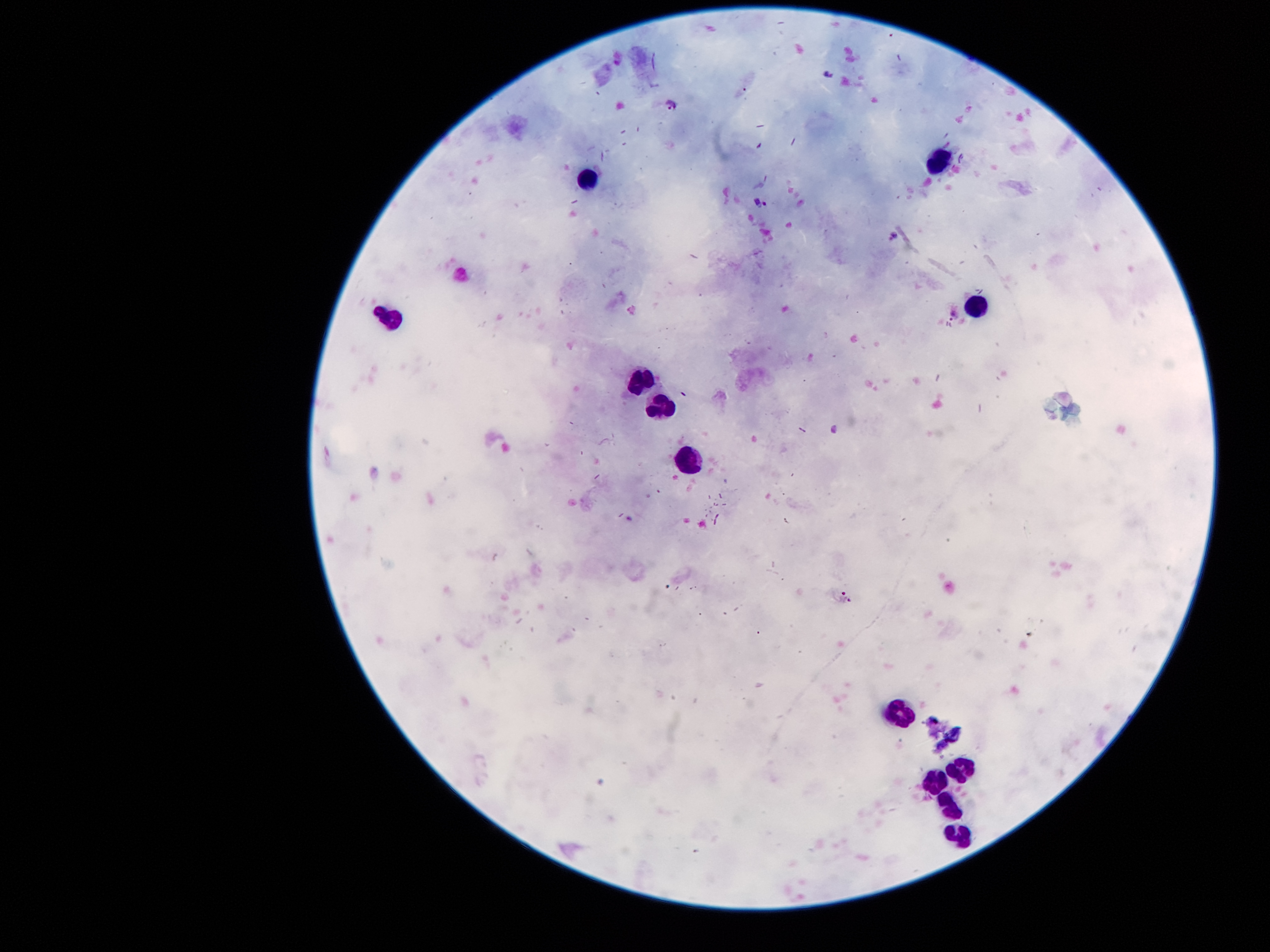

{
  "capture": "smartphone through the microscope eyepiece",
  "stain": "Giemsa",
  "preparation": "thick peripheral-blood smear",
  "patient_malaria_status": "infected with Plasmodium falciparum",
  "leukocyte_locations": "approximate centers as {x, y} in pixels: {937, 161}, {586, 176}, {978, 304}, {390, 316}, {639, 377}, {662, 405}, {695, 461}, {900, 714}, {960, 768}, {939, 781}, {949, 808}, {956, 836}",
  "field_of_view": "one from this slide",
  "magnification": "100x",
  "image_size": "1270×952 pixels",
  "plasmodium_parasite_locations": "approximate centers as {x, y} in pixels: {830, 71}, {671, 105}, {763, 203}, {895, 235}, {954, 317}, {847, 599}"
}